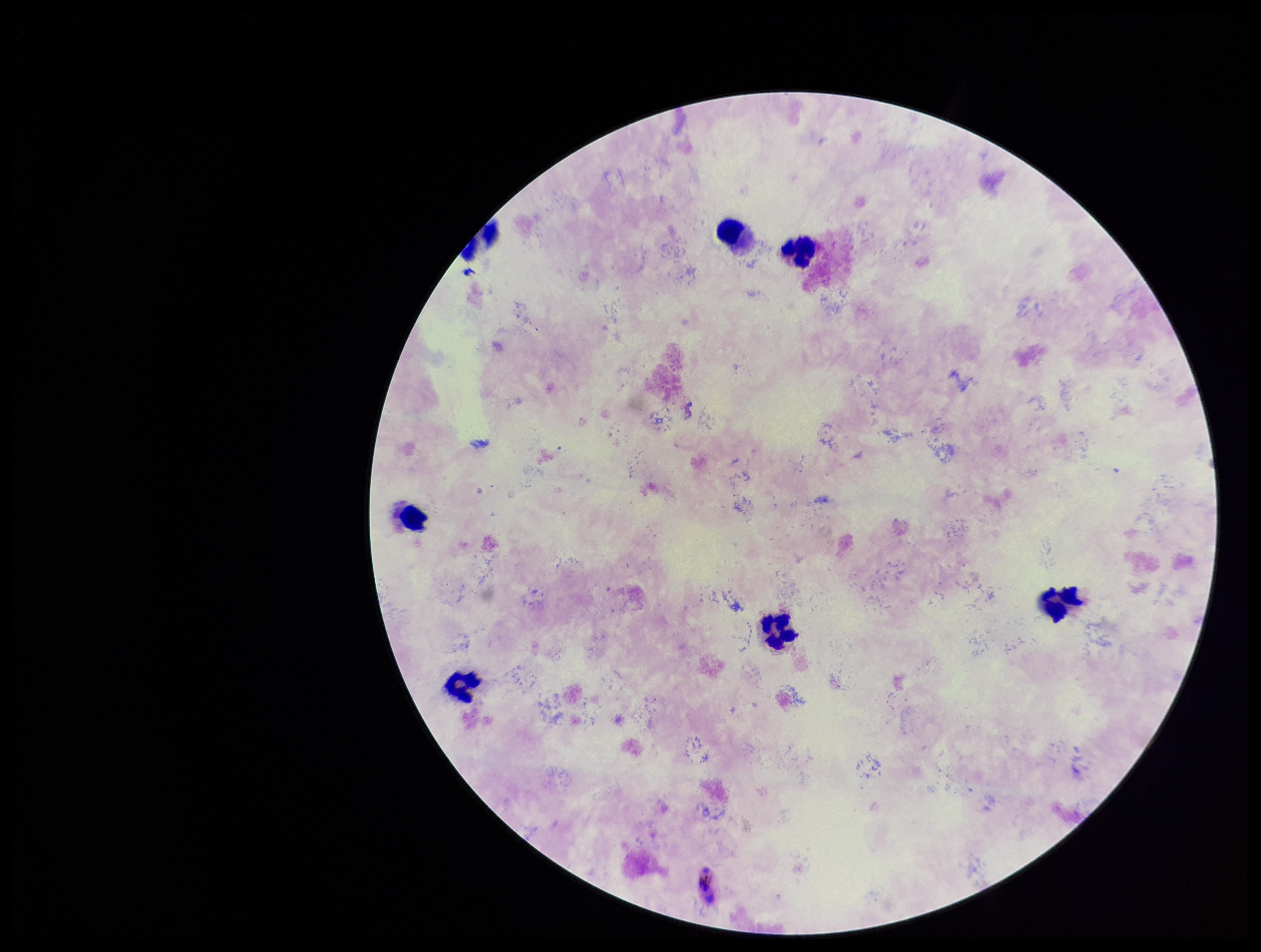
Species reported for this patient: Plasmodium falciparum. Plasmodium parasites: none identified. Parasite count: 0. Preparation: thick smear. Stained with Giemsa. Photographed through the microscope eyepiece with a smartphone camera. Image is 1261×952 pixels. Leukocyte count: 7. Single field of view. Patient malaria status: infected.